State which parasite is depicted.
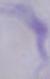
This is a trypanosome.

Photomicrograph. Captured at 1000x magnification.